Locate and identify every blood parasite.
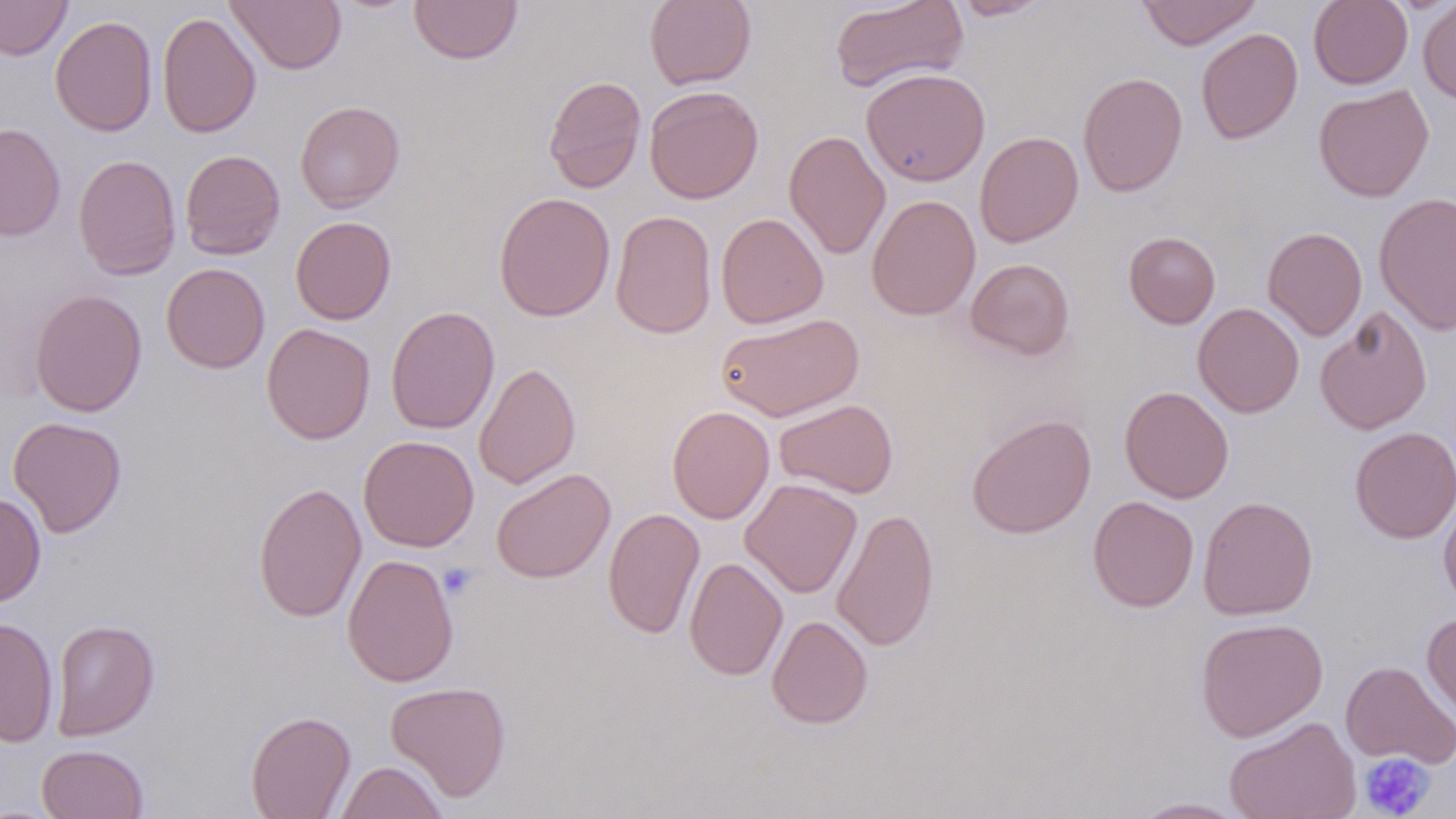

No blood parasites observed.

slide-level diagnosis = negative for blood parasites
magnification = 1000x
modality = light microscopy
image size = 1456×819 pixels
uninfected red blood cell locations = approximate bounding boxes as (x1, y1, x2, y2) in pixels: (0, 0, 72, 60), (409, 0, 523, 65), (645, 0, 756, 90), (830, 0, 969, 93), (948, 0, 1056, 20), (1136, 0, 1262, 50), (1308, 0, 1413, 89), (1418, 0, 1456, 104), (226, 1, 347, 74), (157, 11, 261, 138), (50, 15, 157, 137), (1196, 28, 1302, 144), (861, 68, 990, 186), (1078, 71, 1188, 197), (543, 75, 647, 193), (1313, 84, 1434, 202), (644, 85, 764, 204), (294, 100, 405, 213), (0, 122, 66, 242), (784, 130, 891, 260), (974, 132, 1083, 248), (180, 149, 286, 260), (73, 154, 181, 281), (493, 191, 616, 322), (1374, 192, 1456, 336), (866, 195, 981, 320), (611, 210, 717, 339), (715, 213, 829, 328), (290, 216, 397, 324), (1262, 226, 1367, 340), (1123, 231, 1221, 329), (965, 257, 1075, 361), (161, 263, 270, 373), (29, 289, 148, 417), (1192, 303, 1304, 418), (1315, 304, 1432, 435), (386, 305, 500, 435), (715, 312, 864, 422), (261, 322, 376, 444), (473, 362, 581, 489), (1120, 387, 1234, 503), (774, 398, 898, 498), (667, 405, 774, 524), (966, 413, 1097, 538), (8, 415, 127, 538), (1349, 426, 1455, 543), (358, 435, 479, 552), (490, 468, 615, 583), (740, 478, 862, 598), (252, 481, 367, 623), (0, 491, 46, 606), (1087, 496, 1199, 612), (1198, 496, 1318, 620), (1439, 496, 1456, 615), (603, 507, 705, 638), (831, 507, 939, 651), (342, 553, 459, 687), (684, 557, 788, 681), (1422, 612, 1456, 724), (767, 614, 873, 729), (0, 616, 59, 747), (1195, 617, 1328, 742), (50, 619, 160, 741), (1340, 660, 1456, 769), (385, 681, 512, 802), (245, 710, 356, 819), (1224, 716, 1361, 819), (36, 744, 149, 819), (334, 760, 448, 819), (1128, 797, 1250, 818)
preparation = thin blood smear
stain = May-Grünwald-Giemsa
platelet locations = approximate bounding boxes as (x1, y1, x2, y2) in pixels: (438, 563, 479, 600), (1359, 753, 1436, 818)
field of view = one of a larger specimen